Locate and identify every blood parasite.
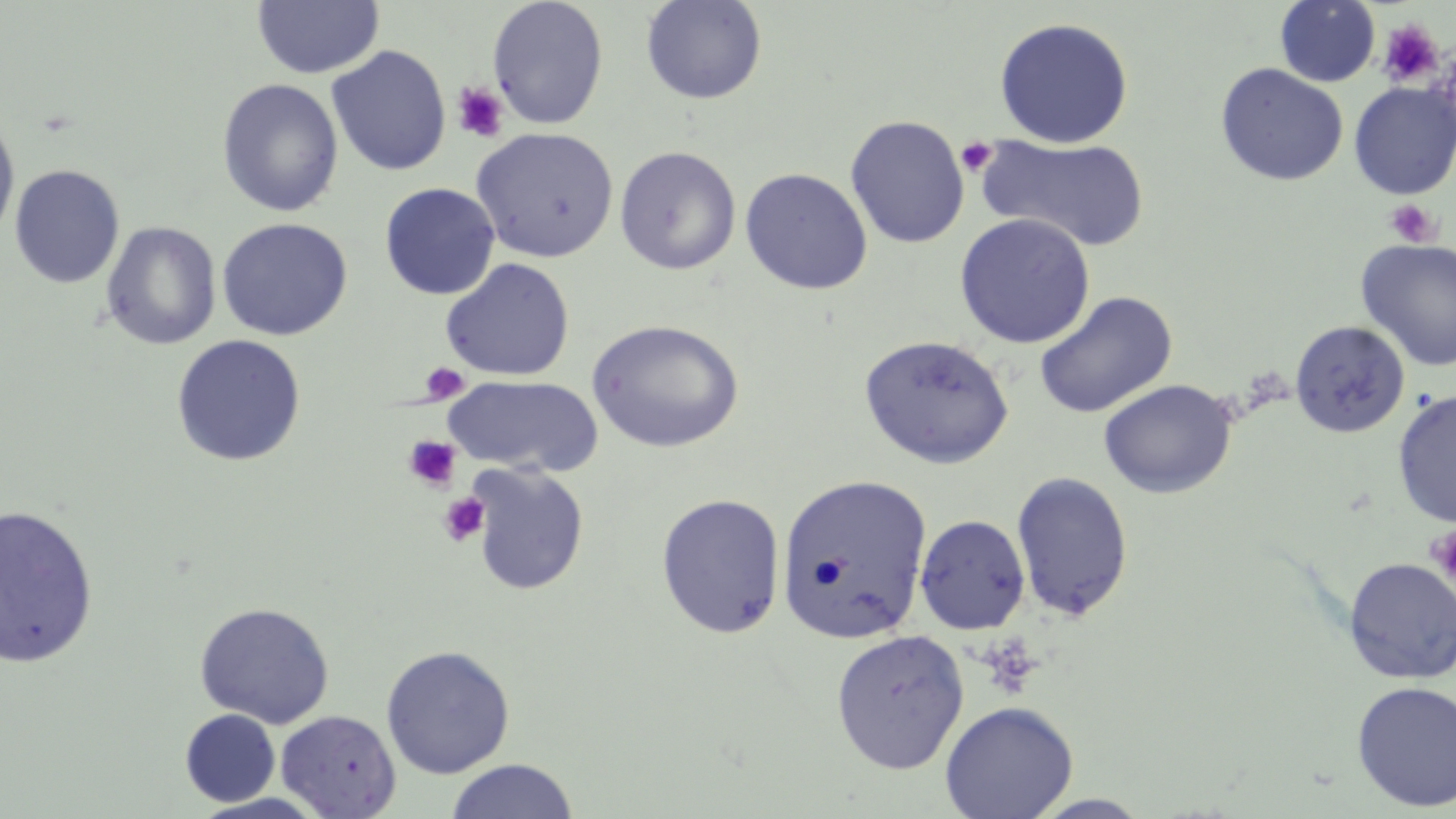
No blood parasites observed.

slide-level diagnosis = negative for blood parasites
magnification = 1000x
modality = light microscopy
platelet locations = approximate bounding boxes as (x1, y1, x2, y2) in pixels: (1377, 19, 1445, 88), (452, 82, 509, 142), (956, 136, 998, 177), (1384, 197, 1441, 247), (420, 362, 470, 404), (402, 435, 462, 492), (438, 492, 490, 546), (1427, 525, 1456, 586)
image size = 1456×819 pixels
uninfected red blood cell locations = approximate bounding boxes as (x1, y1, x2, y2) in pixels: (253, 0, 384, 80), (487, 0, 608, 129), (641, 0, 768, 105), (1275, 0, 1380, 87), (994, 17, 1133, 148), (326, 46, 451, 176), (1214, 63, 1348, 187), (216, 78, 344, 217), (1349, 81, 1456, 199), (0, 112, 20, 247), (845, 115, 969, 249), (471, 127, 619, 263), (978, 135, 1151, 253), (614, 146, 741, 275), (9, 165, 125, 289), (739, 168, 873, 295), (379, 182, 500, 300), (954, 213, 1095, 348), (216, 217, 353, 341), (100, 221, 221, 351), (1354, 238, 1456, 372), (440, 258, 575, 381), (1034, 291, 1177, 418), (587, 319, 745, 453), (1288, 319, 1411, 439), (170, 334, 307, 467), (859, 334, 1014, 469), (443, 375, 603, 477), (1098, 379, 1237, 499), (1392, 388, 1456, 528), (465, 462, 590, 596), (1011, 471, 1134, 621), (776, 473, 932, 644), (656, 493, 786, 639), (0, 503, 98, 670), (914, 514, 1031, 634), (1343, 557, 1456, 685), (194, 601, 335, 729), (830, 628, 969, 773), (380, 644, 515, 779), (1351, 680, 1456, 812), (939, 700, 1079, 819), (180, 709, 280, 807), (275, 709, 401, 818), (445, 759, 580, 818), (188, 792, 334, 818), (1026, 793, 1155, 818)
preparation = thin blood smear
stain = May-Grünwald-Giemsa
field of view = single